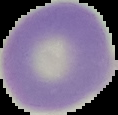 Image is 118×115 pixels. From a thin blood film. Malaria status: uninfected. Segmented cell region on a black background.